Assess this cell for malaria.
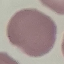

It is uninfected.

capture = smartphone camera at the microscope eyepiece
image type = cell patch, automatically extracted from a larger field of view and resized to 64 × 64 pixels
preparation = thin blood smear
stain = Giemsa